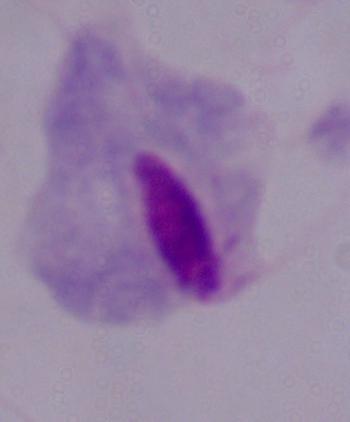
identification: trichomonad
magnification: 1000x
modality: photomicrograph